Assess this cell for malaria.
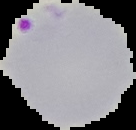
It is parasitized.

Summary:
  - Image type: segmented cell region on a black background
  - Preparation: thin blood film
  - Image size: 136×130 pixels